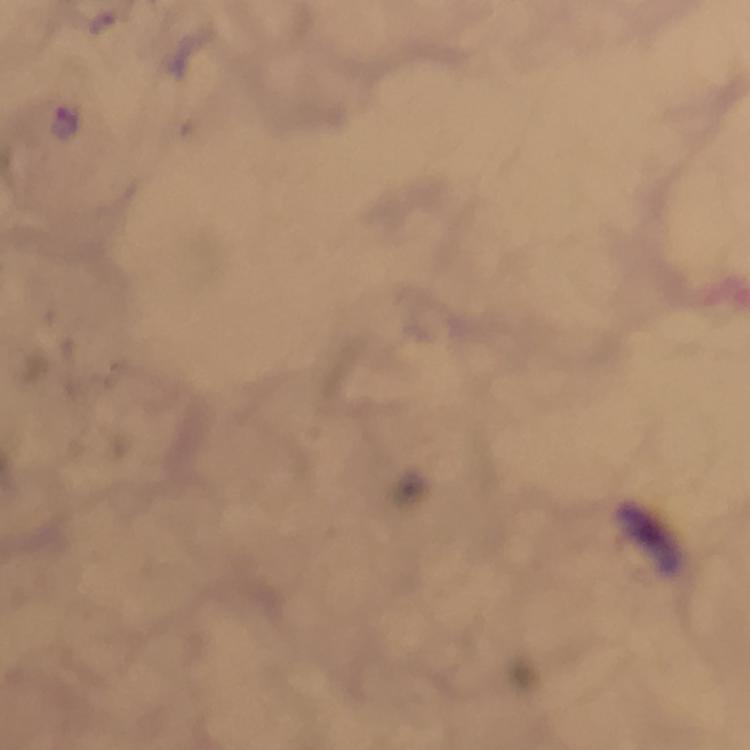

Approximate centers as (x, y) in pixels. Plasmodium parasite locations: (64, 123). Thick blood film. Immersion oil applied. Cropped region of a single field of view. Image is 750×750 pixels. Photographed through the microscope with a smartphone camera. Giemsa stain. From a malaria diagnostic workup. At 100x magnification.